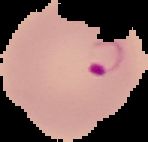
Summary:
  - Image type: cell region segmented out of the field of view; surrounding area masked to black
  - Image size: 148×142 pixels
  - Preparation: thin blood smear
  - Result: malaria parasites identified